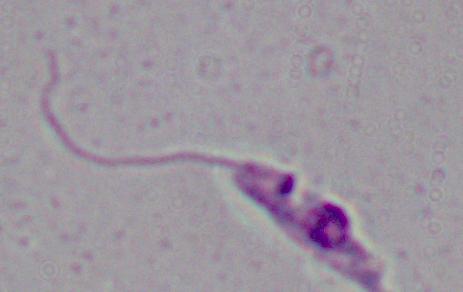

Photomicrograph. 1000x magnification. A Leishmania parasite is shown.